Look for Plasmodium parasites.
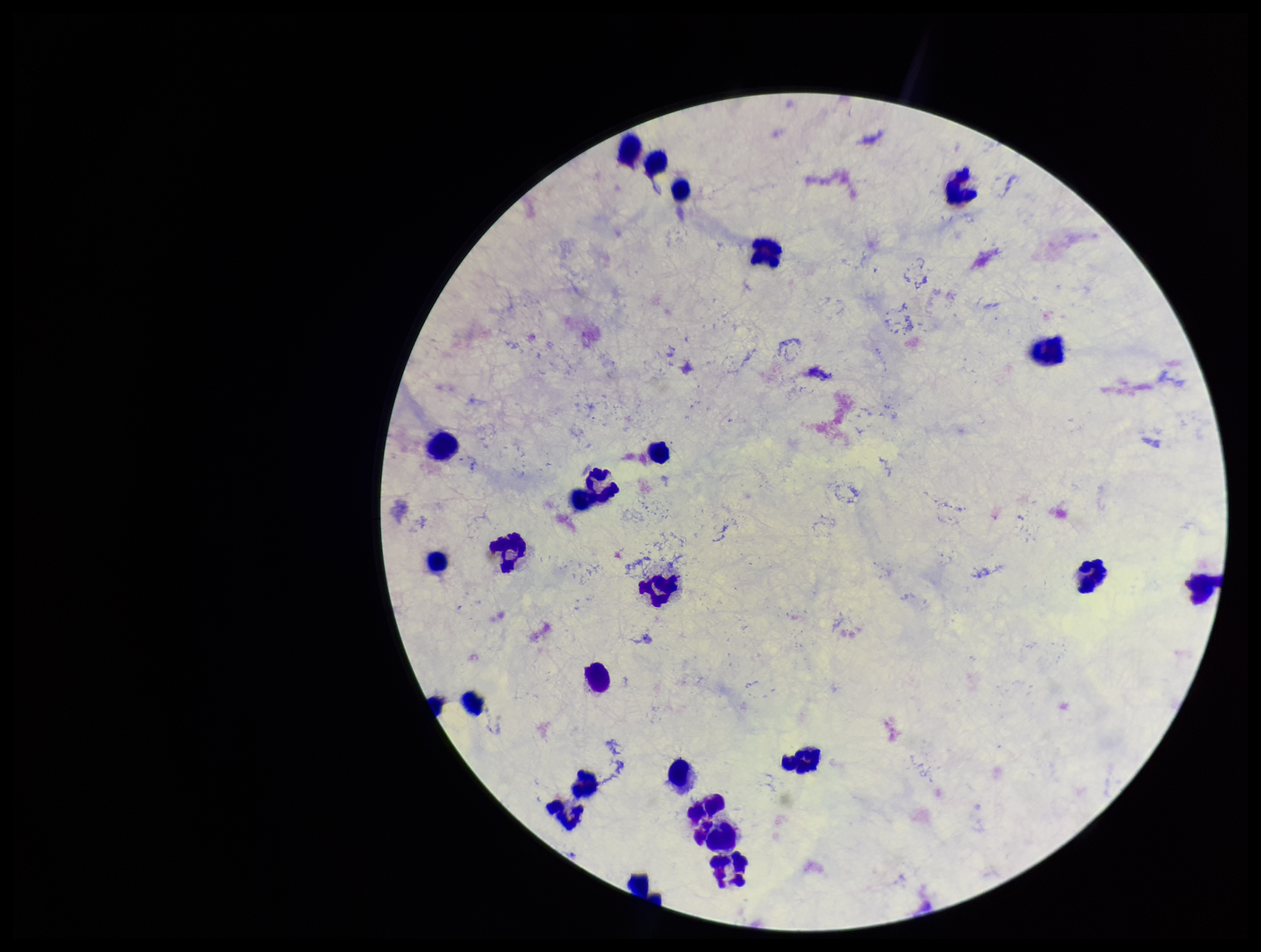

None identified.

Smartphone photograph taken through the eyepiece of a microscope. One field from this slide. Patient malaria status: negative. Image is 1261×952 pixels. Leukocyte count: 24. Stained with Giemsa. Parasite count: 0. Preparation: thick.